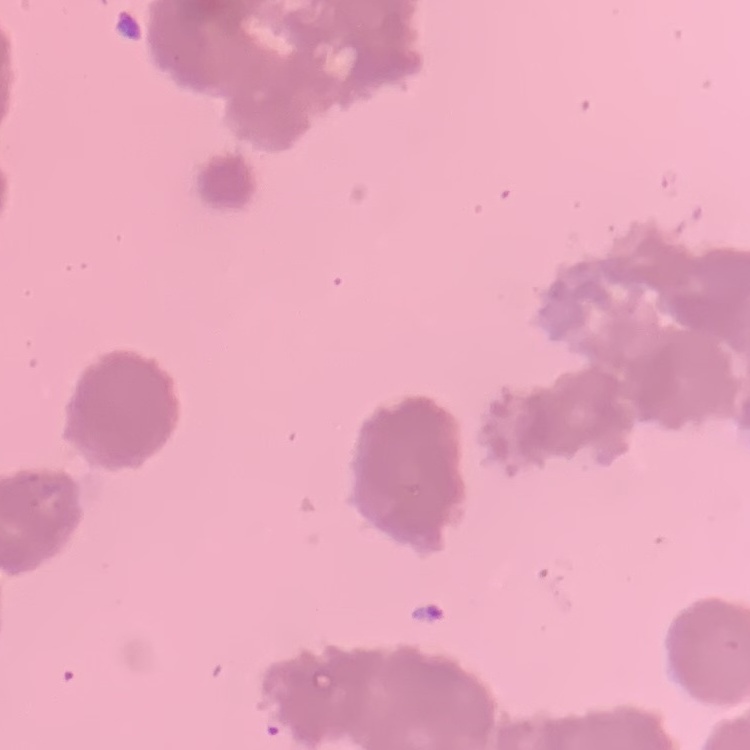

Summary:
  - Erythrocyte morphology: rouleaux formation
  - Stain: Field's or Giemsa
  - Preparation: thin blood film
  - Image type: square crop of a larger photomicrograph